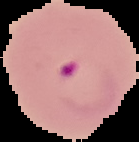

Summary:
  - Preparation: thin blood film
  - Result: Plasmodium parasites detected
  - Image type: cell region segmented out of the field of view; surrounding area masked to black
  - Image size: 139×142 pixels